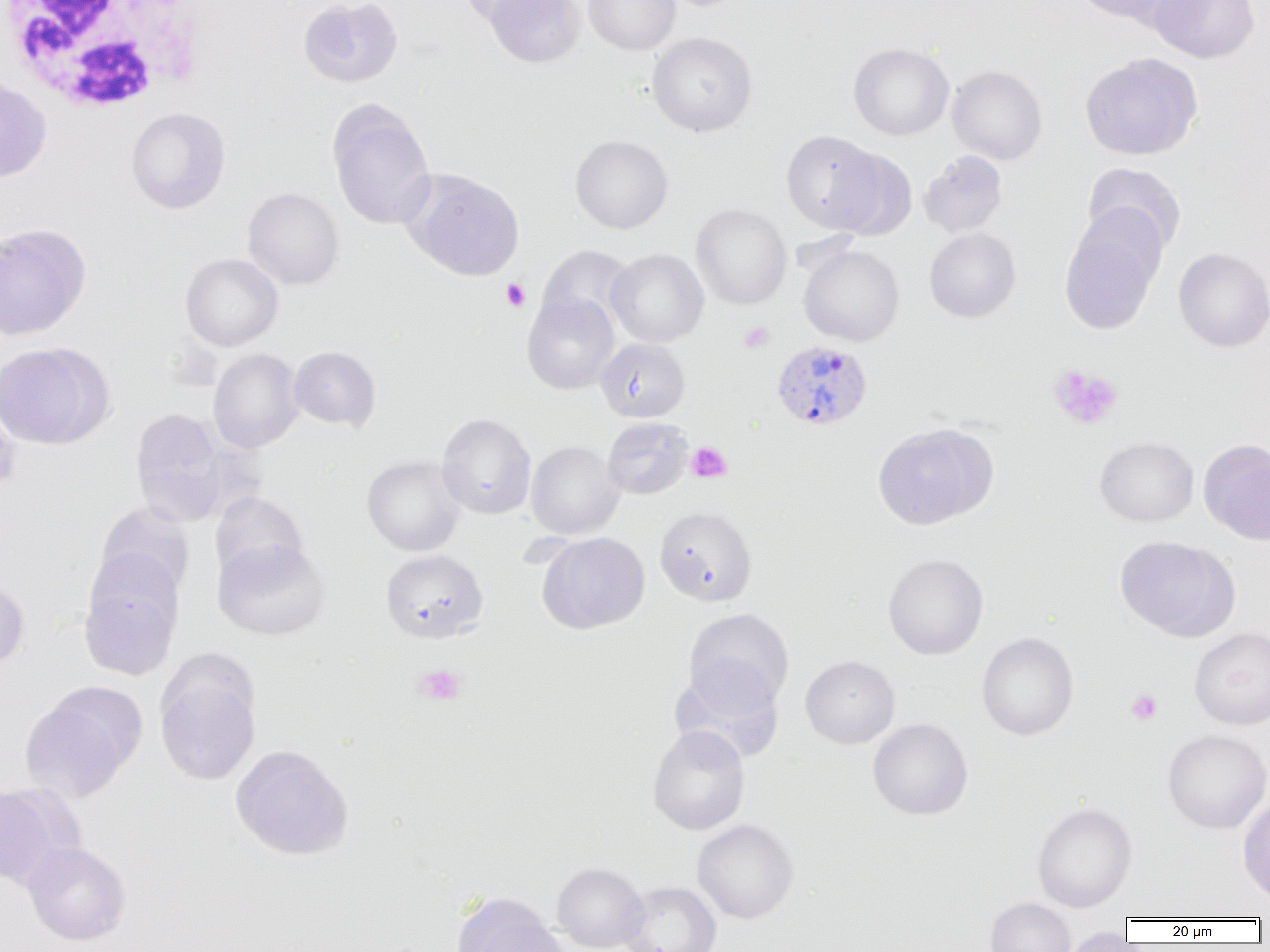
Summary:
  - Coordinate format: approximate bounding boxes as (x1, y1, x2, y2) in pixels
  - Plasmodium vivax-infected red blood cell locations: (772, 339, 873, 432)
  - White blood cell locations: (1, 1, 210, 113)
  - Uninfected red blood cell locations: (298, 0, 402, 87), (460, 0, 556, 27), (485, 0, 585, 68), (583, 0, 680, 55), (1070, 0, 1176, 24), (1147, 0, 1260, 63), (646, 32, 758, 137), (848, 42, 954, 141), (1080, 52, 1202, 160), (947, 65, 1048, 165), (0, 75, 51, 182), (327, 99, 436, 230), (126, 107, 230, 213), (781, 130, 883, 232), (570, 135, 673, 233), (827, 147, 917, 241), (918, 150, 1008, 237), (1082, 162, 1186, 256), (405, 169, 525, 281), (243, 187, 344, 289), (691, 203, 791, 309), (1059, 216, 1162, 335), (0, 223, 91, 341), (924, 227, 1021, 323), (538, 245, 635, 333), (799, 245, 904, 346), (1173, 247, 1270, 352), (606, 249, 709, 347), (180, 253, 283, 351), (521, 293, 619, 394), (596, 338, 690, 422), (0, 342, 111, 449), (288, 345, 381, 432), (208, 348, 304, 454), (0, 396, 20, 498), (130, 408, 229, 525), (436, 413, 536, 519), (602, 417, 693, 500), (872, 423, 997, 530), (1094, 436, 1199, 526), (1198, 439, 1270, 545), (526, 441, 624, 539), (362, 455, 466, 556), (210, 492, 307, 581), (94, 503, 195, 602), (655, 506, 756, 606), (537, 532, 650, 634), (1115, 536, 1239, 641), (212, 538, 330, 640), (381, 549, 488, 643), (883, 553, 988, 659), (79, 557, 183, 681), (0, 579, 29, 672), (683, 608, 794, 711), (1189, 627, 1270, 730), (977, 632, 1078, 741), (800, 656, 900, 748), (155, 661, 261, 786), (670, 664, 784, 762), (19, 691, 139, 803), (868, 718, 973, 820), (647, 724, 750, 835), (1162, 729, 1270, 833), (230, 744, 354, 861), (0, 783, 62, 889), (1237, 794, 1270, 908), (1031, 802, 1138, 912), (692, 819, 798, 924), (22, 841, 130, 944), (552, 862, 648, 951), (621, 881, 722, 952), (453, 894, 565, 952), (985, 897, 1075, 952), (1060, 927, 1134, 952)
  - Platelet locations: (501, 278, 530, 312), (739, 322, 774, 352), (1047, 364, 1123, 430), (686, 442, 732, 483), (413, 664, 466, 705), (1126, 689, 1162, 725)
  - Slide-level diagnosis: Plasmodium vivax
  - Magnification: 1000x
  - Preparation: thin blood smear
  - Image size: 1270×952 pixels
  - Modality: optical microscopy
  - Field of view: one of a larger specimen